Classify the preparation.
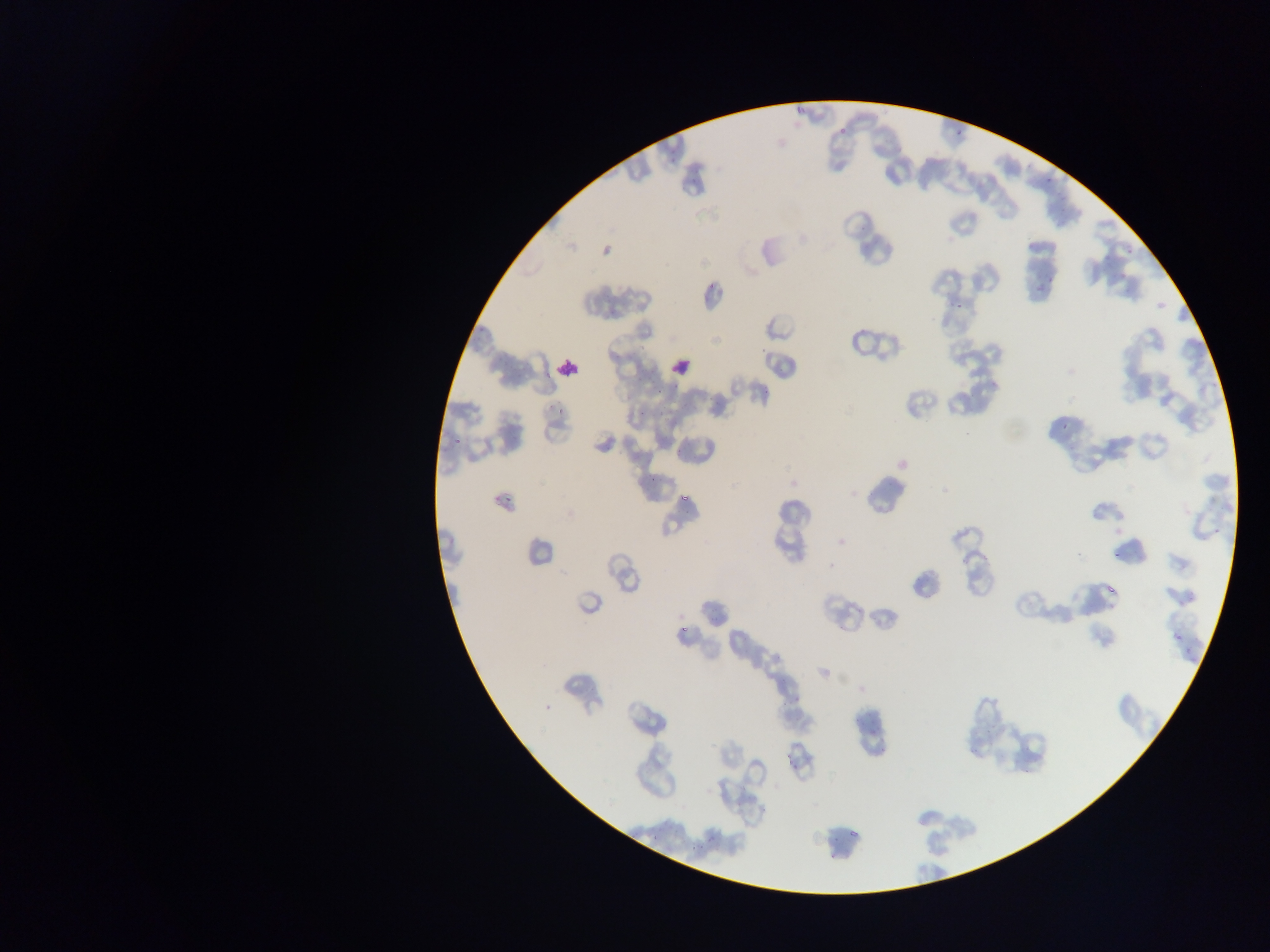

Thin blood film.

Approximate bounding boxes as (left, top, right, bottom) in pixels.
Summary:
  - Leukocyte locations: (664, 352, 695, 383), (553, 353, 584, 384)
  - Plasmodium parasite locations: (794, 104, 807, 117), (837, 125, 849, 138), (949, 126, 967, 136), (666, 145, 688, 162), (686, 170, 702, 185), (1043, 176, 1049, 187), (705, 274, 723, 300), (1047, 275, 1061, 286), (950, 299, 965, 309), (760, 386, 772, 397), (651, 399, 671, 420), (556, 406, 565, 419), (1063, 415, 1073, 432), (449, 424, 467, 446), (648, 472, 669, 482), (679, 493, 692, 505), (502, 496, 512, 506), (1211, 524, 1225, 534), (1110, 547, 1126, 564), (1106, 583, 1119, 604), (675, 616, 692, 631), (1173, 632, 1183, 640), (1181, 649, 1193, 659), (540, 699, 553, 709), (779, 743, 800, 772), (687, 832, 721, 846) | approximate (x, y) pixel centers of objects too small to bound: (766, 346)
  - Capture: mobile-phone photograph through a microscope
  - Country: Ghana
  - Field of view: single
  - Image size: 1270×952 pixels